Classify this cell by malaria status.
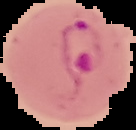

It is parasitized.

image size = 136×130 pixels
preparation = thin blood smear
image type = cell region segmented out of the field of view; surrounding area masked to black